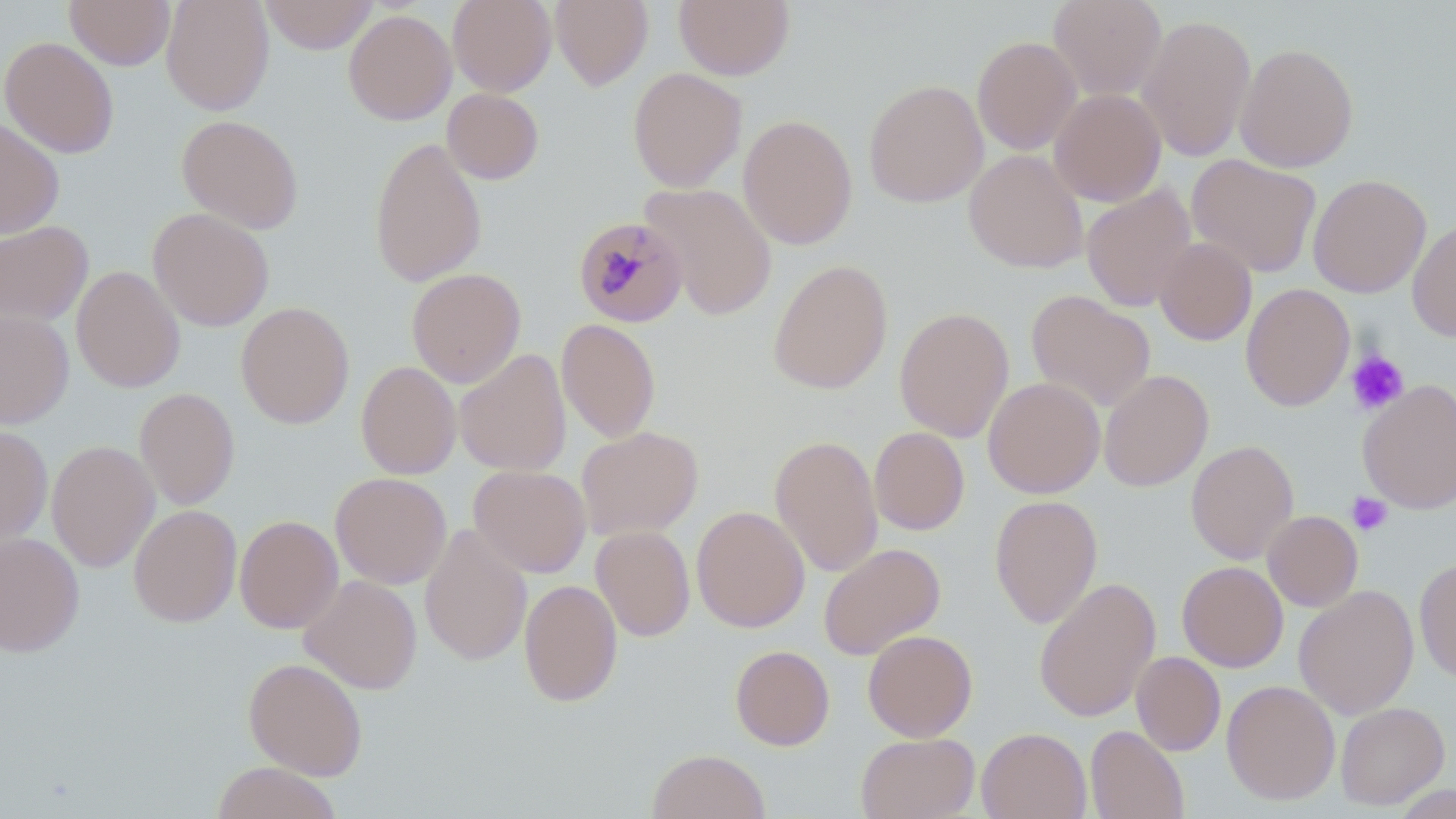
slide-level diagnosis = Plasmodium malariae
uninfected red blood cell locations = approximate bounding boxes as (x1,y1)-(x2,y2) corner pairs in pixels: (65,0)-(175,70), (161,0)-(274,115), (259,0)-(379,54), (448,0)-(557,96), (551,0)-(652,90), (674,0)-(795,80), (1047,0)-(1167,101), (343,9)-(457,125), (1136,13)-(1257,162), (972,35)-(1082,155), (1,36)-(120,158), (1235,42)-(1359,172), (627,67)-(747,191), (864,79)-(988,207), (442,88)-(544,184), (1049,88)-(1166,206), (176,114)-(304,233), (738,114)-(858,250), (0,117)-(65,238), (369,136)-(487,288), (964,149)-(1088,273), (1186,153)-(1322,278), (1307,174)-(1432,298), (640,182)-(778,320), (1080,184)-(1198,312), (148,208)-(275,331), (1407,219)-(1456,341), (0,220)-(94,327), (1154,237)-(1257,345), (768,259)-(893,394), (71,265)-(185,393), (406,268)-(526,388), (1241,283)-(1356,411), (1026,290)-(1155,412), (236,301)-(355,428), (894,306)-(1014,443), (0,309)-(74,428), (556,319)-(660,442), (455,348)-(572,477), (356,360)-(462,479), (1098,369)-(1214,492), (983,377)-(1105,498), (1357,379)-(1456,514), (134,387)-(240,510), (0,424)-(53,546), (576,426)-(703,540), (869,427)-(970,535), (770,434)-(883,577), (46,440)-(160,572), (1185,440)-(1299,565), (469,465)-(591,578), (330,471)-(451,589), (989,494)-(1103,629), (128,504)-(241,627), (691,505)-(810,632), (1263,510)-(1363,611), (235,515)-(343,634), (419,523)-(533,667), (591,525)-(695,641), (0,532)-(84,657), (819,542)-(945,660), (1414,558)-(1456,684), (1177,561)-(1288,672), (299,575)-(422,694), (1033,576)-(1161,723), (519,578)-(623,708), (1294,585)-(1419,718), (862,629)-(978,742), (730,645)-(835,750), (1131,651)-(1226,756), (243,657)-(368,780), (1222,680)-(1340,804), (1335,701)-(1450,809), (1085,725)-(1189,819), (976,727)-(1091,819), (856,732)-(979,819), (646,749)-(771,819), (210,762)-(343,819)
image size = 1456×819 pixels
field of view = single
preparation = thin blood smear
platelet locations = approximate bounding boxes as (x1,y1)-(x2,y2) corner pairs in pixels: (1345,349)-(1409,416), (1347,492)-(1393,536)
Plasmodium malariae-infected red blood cell locations = approximate bounding boxes as (x1,y1)-(x2,y2) corner pairs in pixels: (573,216)-(688,328)
modality = optical microscopy
stain = May-Grünwald-Giemsa
magnification = 1000x